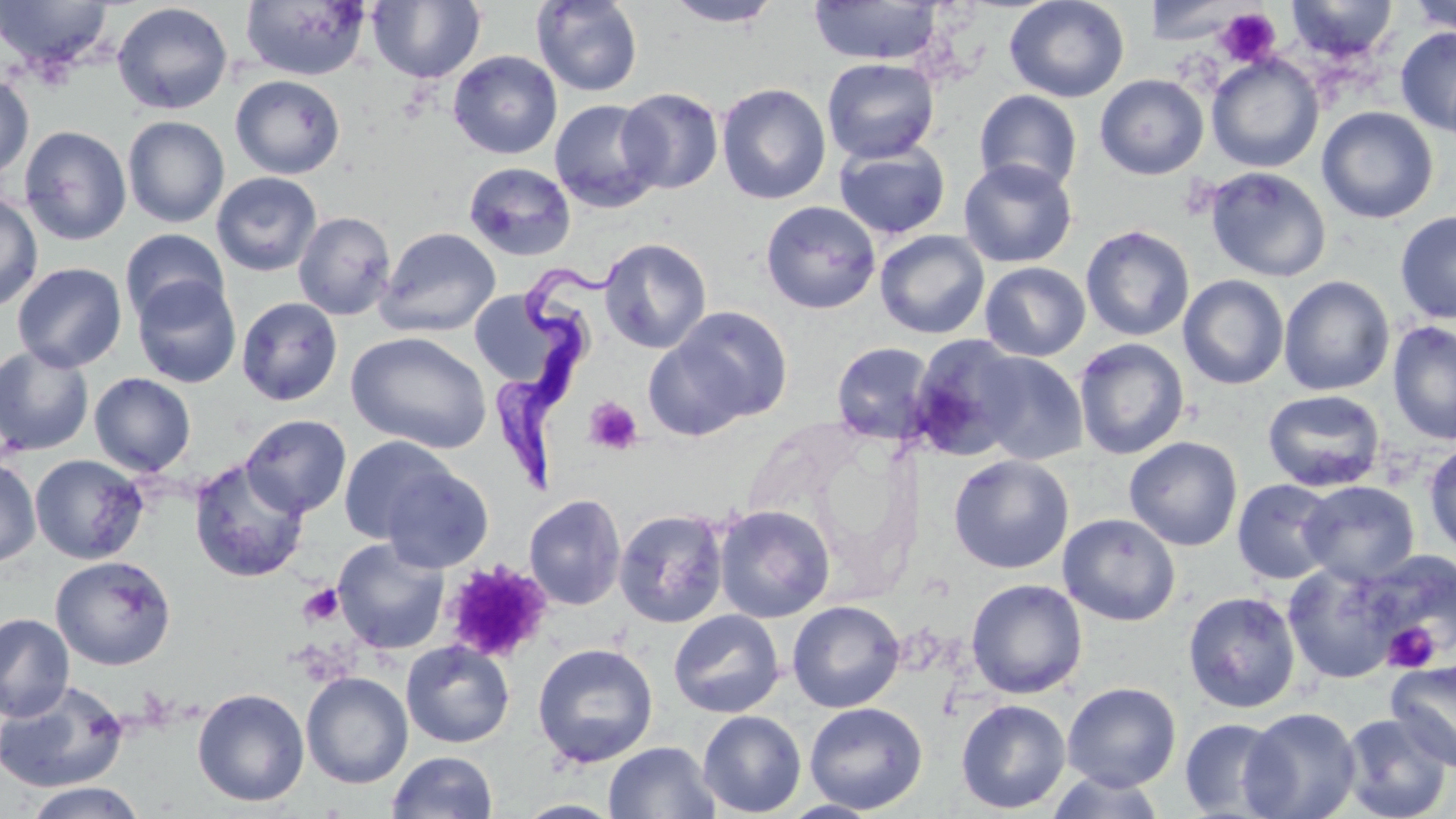 Approximate bounding boxes as named x1/y1/x2/y2 corners in pixels. Uninfected red blood cell locations: (x1=0, y1=0, x2=115, y2=75), (x1=240, y1=0, x2=371, y2=81), (x1=368, y1=0, x2=485, y2=84), (x1=664, y1=0, x2=785, y2=28), (x1=1004, y1=0, x2=1130, y2=103), (x1=1285, y1=0, x2=1399, y2=61), (x1=1405, y1=0, x2=1456, y2=36), (x1=531, y1=1, x2=643, y2=97), (x1=808, y1=1, x2=944, y2=66), (x1=1147, y1=1, x2=1242, y2=44), (x1=112, y1=2, x2=233, y2=115), (x1=1396, y1=27, x2=1456, y2=135), (x1=448, y1=50, x2=562, y2=159), (x1=1206, y1=54, x2=1324, y2=173), (x1=822, y1=57, x2=940, y2=164), (x1=0, y1=74, x2=34, y2=181), (x1=1095, y1=74, x2=1209, y2=179), (x1=231, y1=75, x2=345, y2=179), (x1=716, y1=83, x2=832, y2=205), (x1=617, y1=87, x2=724, y2=195), (x1=974, y1=89, x2=1083, y2=195), (x1=549, y1=100, x2=663, y2=213), (x1=1317, y1=107, x2=1438, y2=224), (x1=122, y1=116, x2=230, y2=228), (x1=19, y1=125, x2=132, y2=245), (x1=833, y1=140, x2=951, y2=240), (x1=958, y1=158, x2=1077, y2=269), (x1=464, y1=162, x2=576, y2=260), (x1=1204, y1=167, x2=1332, y2=282), (x1=211, y1=172, x2=322, y2=276), (x1=0, y1=191, x2=43, y2=312), (x1=760, y1=200, x2=882, y2=314), (x1=1395, y1=211, x2=1456, y2=324), (x1=293, y1=212, x2=396, y2=320), (x1=1080, y1=225, x2=1195, y2=342), (x1=377, y1=227, x2=501, y2=337), (x1=120, y1=228, x2=229, y2=325), (x1=874, y1=230, x2=990, y2=340), (x1=598, y1=237, x2=712, y2=354), (x1=12, y1=262, x2=127, y2=372), (x1=979, y1=262, x2=1090, y2=362), (x1=1178, y1=274, x2=1290, y2=390), (x1=1278, y1=275, x2=1395, y2=397), (x1=132, y1=276, x2=242, y2=388), (x1=469, y1=290, x2=558, y2=384), (x1=236, y1=296, x2=343, y2=406), (x1=663, y1=306, x2=793, y2=428), (x1=1387, y1=321, x2=1456, y2=446), (x1=347, y1=331, x2=492, y2=454), (x1=643, y1=335, x2=755, y2=441), (x1=907, y1=335, x2=1030, y2=462), (x1=1074, y1=338, x2=1190, y2=460), (x1=831, y1=341, x2=937, y2=445), (x1=0, y1=345, x2=94, y2=456), (x1=970, y1=350, x2=1088, y2=465), (x1=89, y1=373, x2=196, y2=476), (x1=1262, y1=389, x2=1386, y2=492), (x1=241, y1=414, x2=352, y2=518), (x1=338, y1=435, x2=455, y2=543), (x1=1124, y1=435, x2=1243, y2=551), (x1=1423, y1=442, x2=1456, y2=556), (x1=30, y1=454, x2=149, y2=564), (x1=948, y1=454, x2=1074, y2=573), (x1=0, y1=458, x2=41, y2=567), (x1=189, y1=459, x2=310, y2=583), (x1=380, y1=465, x2=493, y2=572), (x1=1233, y1=479, x2=1340, y2=584), (x1=1298, y1=480, x2=1420, y2=586), (x1=524, y1=494, x2=626, y2=610), (x1=714, y1=505, x2=835, y2=623), (x1=614, y1=508, x2=730, y2=628), (x1=1058, y1=513, x2=1181, y2=626), (x1=332, y1=538, x2=449, y2=655), (x1=1359, y1=551, x2=1456, y2=666), (x1=50, y1=555, x2=176, y2=670), (x1=1282, y1=562, x2=1401, y2=685), (x1=966, y1=579, x2=1088, y2=699), (x1=1182, y1=590, x2=1302, y2=714), (x1=787, y1=601, x2=905, y2=713), (x1=669, y1=609, x2=786, y2=718), (x1=0, y1=612, x2=74, y2=723), (x1=401, y1=641, x2=515, y2=748), (x1=532, y1=642, x2=658, y2=768), (x1=1387, y1=660, x2=1456, y2=772), (x1=301, y1=671, x2=413, y2=789), (x1=0, y1=679, x2=130, y2=793), (x1=1062, y1=682, x2=1181, y2=791), (x1=192, y1=687, x2=309, y2=806), (x1=955, y1=699, x2=1071, y2=814), (x1=804, y1=702, x2=928, y2=814), (x1=1240, y1=706, x2=1362, y2=819), (x1=698, y1=710, x2=806, y2=817), (x1=1339, y1=712, x2=1453, y2=819), (x1=1179, y1=717, x2=1290, y2=818), (x1=604, y1=741, x2=720, y2=819), (x1=387, y1=750, x2=498, y2=819), (x1=1045, y1=772, x2=1168, y2=818), (x1=21, y1=782, x2=147, y2=818), (x1=513, y1=799, x2=624, y2=818), (x1=778, y1=799, x2=885, y2=818). Trypanosoma brucei locations: (x1=493, y1=259, x2=626, y2=490). Platelet locations: (x1=1215, y1=7, x2=1282, y2=68), (x1=583, y1=396, x2=643, y2=455), (x1=442, y1=560, x2=553, y2=662), (x1=297, y1=583, x2=344, y2=627), (x1=1382, y1=622, x2=1440, y2=672). Slide-level diagnosis: Trypanosoma brucei. Thin blood film. May-Grünwald-Giemsa-stained preparation. Optical microscopy. One field of a larger specimen. Image is 1456×819 pixels. Captured at 1000x magnification.